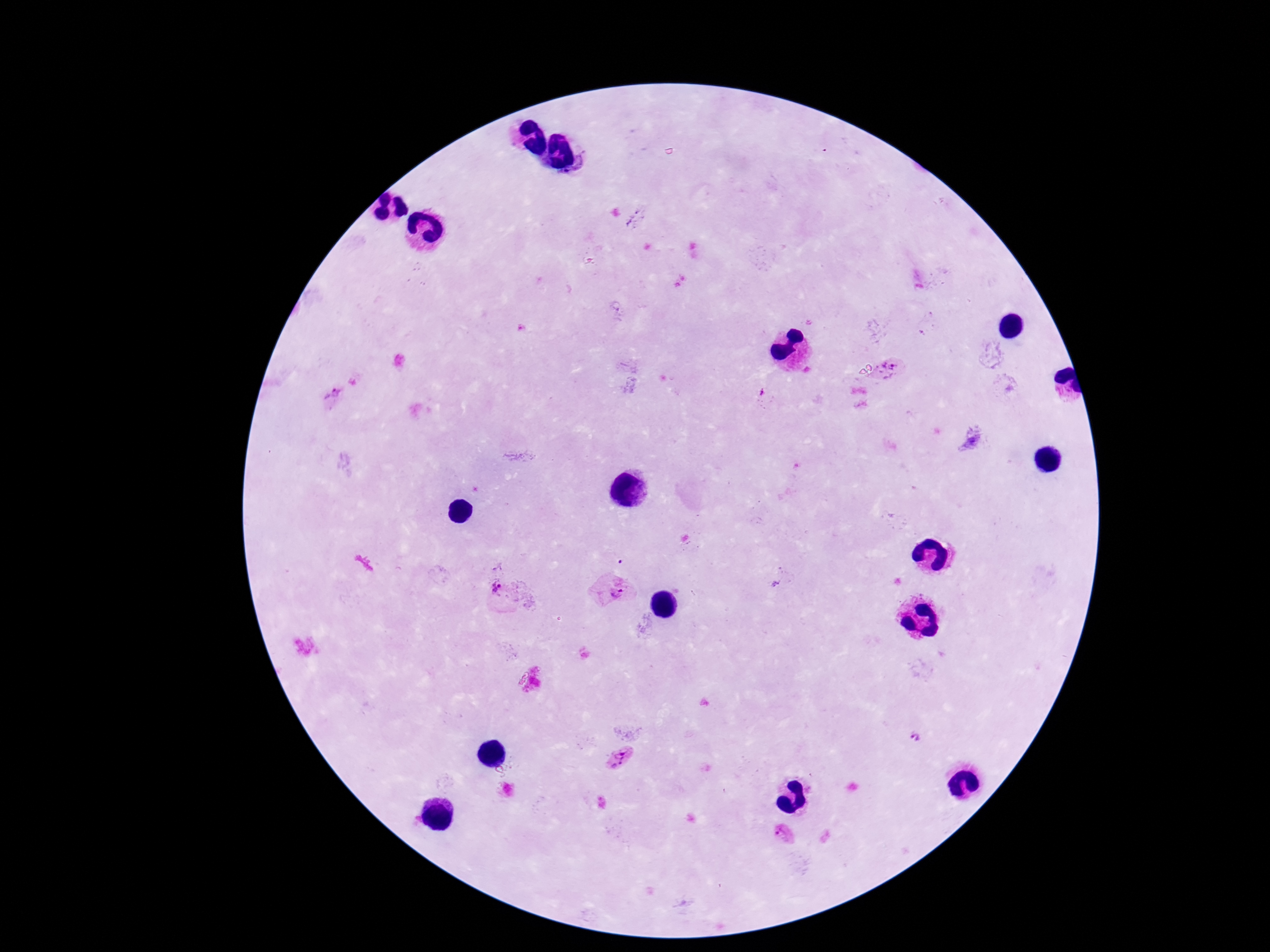

Plasmodium parasite locations = approximate centers as {x, y} in pixels: {572, 161}, {892, 370}, {335, 394}, {971, 440}, {499, 590}, {614, 591}, {918, 737}, {620, 759}, {783, 833}
image size = 1270×952 pixels
preparation = thick blood smear
capture = smartphone camera through the microscope eyepiece
patient malaria status = positive
field of view = one from this slide
stain = Giemsa
magnification = 100x